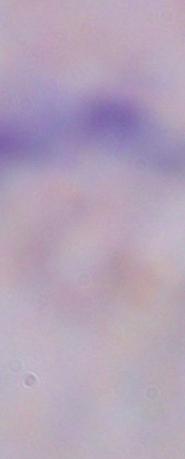
magnification = 1000x
identification = trypanosome
modality = micrograph